Assess the morphology of the erythrocytes.
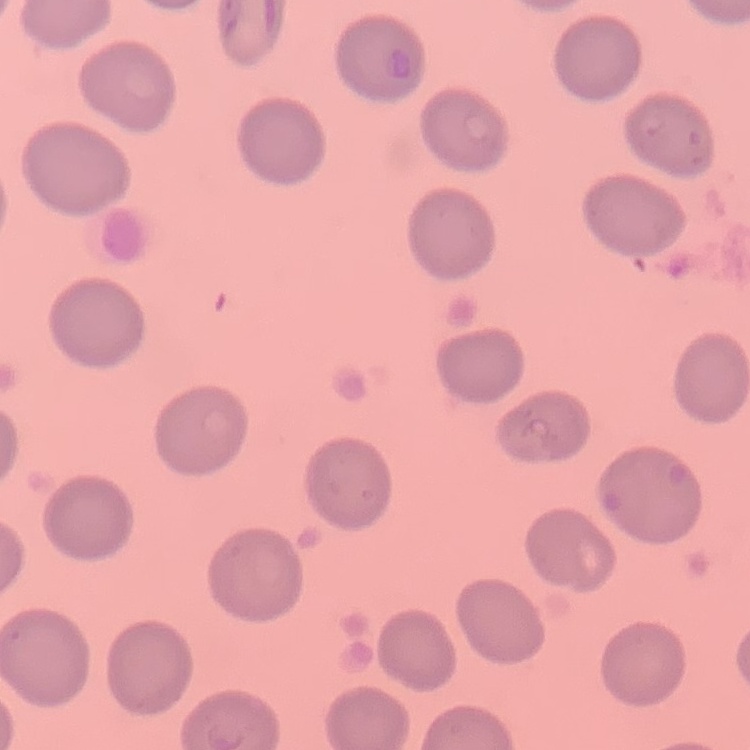
They show no rouleaux formation.

Square crop of a larger photomicrograph. Thin blood smear. Field's or Giemsa stain.